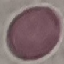
Malaria status: uninfected. Photographed with a smartphone camera at the microscope eyepiece. Thin blood smear. Cell patch, automatically extracted from a larger field of view and resized to 64 × 64 pixels. Giemsa-stained preparation.